Locate every blood parasite and identify its species.
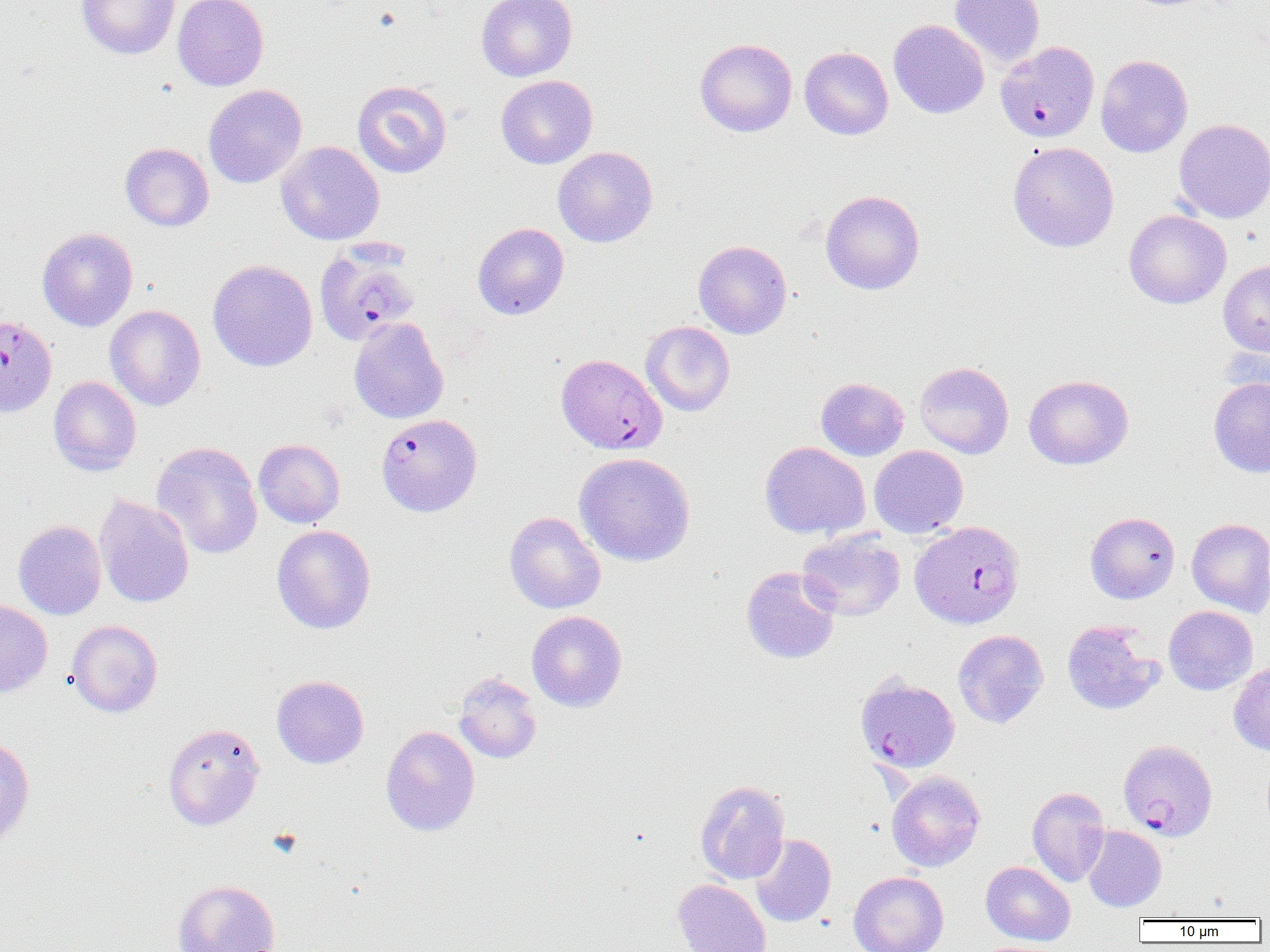

Approximate bounding boxes as (x1,y1)-(x2,y2) corner pairs in pixels.
Plasmodium falciparum-infected red blood cells: (997,39)-(1101,144), (314,244)-(422,345), (0,315)-(57,416), (556,353)-(666,455), (376,413)-(482,517), (910,520)-(1025,628), (854,673)-(960,773), (1117,739)-(1218,842).
No Plasmodium ovale, Plasmodium malariae, Plasmodium vivax, Babesia divergens, or Trypanosoma brucei observed.

Summary:
  - Uninfected red blood cell locations: (76,0)-(180,59), (173,0)-(269,91), (476,0)-(578,81), (950,0)-(1045,67), (888,19)-(989,118), (695,38)-(797,137), (800,47)-(893,140), (1095,54)-(1192,157), (496,75)-(598,169), (352,80)-(452,178), (203,84)-(307,188), (1174,118)-(1270,223), (276,141)-(385,245), (1008,141)-(1119,252), (120,142)-(214,231), (552,146)-(658,247), (820,189)-(924,295), (1123,209)-(1231,309), (472,222)-(569,320), (37,227)-(138,331), (693,240)-(792,339), (208,259)-(317,372), (1218,260)-(1270,357), (105,304)-(205,411), (349,317)-(449,424), (641,321)-(735,416), (915,361)-(1014,458), (1024,375)-(1133,470), (48,376)-(141,476), (816,377)-(909,460), (1209,377)-(1270,477), (253,438)-(345,528), (152,441)-(263,559), (760,441)-(870,539), (869,445)-(968,537), (574,452)-(695,566), (94,494)-(195,609), (504,511)-(606,614), (1085,512)-(1180,604), (1186,518)-(1270,617), (13,520)-(106,619), (272,525)-(376,634), (796,530)-(905,621), (741,566)-(841,664), (0,599)-(52,699), (1164,605)-(1257,695), (527,610)-(627,712), (67,620)-(163,717), (1062,620)-(1164,715), (953,629)-(1048,728), (1228,662)-(1270,756), (453,672)-(542,763), (272,675)-(369,768), (162,723)-(265,830), (380,725)-(480,836), (0,735)-(35,852), (886,770)-(985,872), (695,780)-(790,884), (1027,786)-(1110,886), (1082,826)-(1166,912), (750,834)-(836,927), (981,861)-(1075,946), (849,871)-(949,952), (173,879)-(280,952), (672,879)-(771,952)
  - Slide-level diagnosis: Plasmodium falciparum
  - Image size: 1270×952 pixels
  - Modality: optical microscopy
  - Field of view: single
  - Magnification: 1000x
  - Preparation: thin blood film